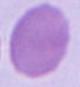 Captured at 1000x magnification. Photomicrograph. A red blood cell is seen.